Describe the morphology of the erythrocytes.
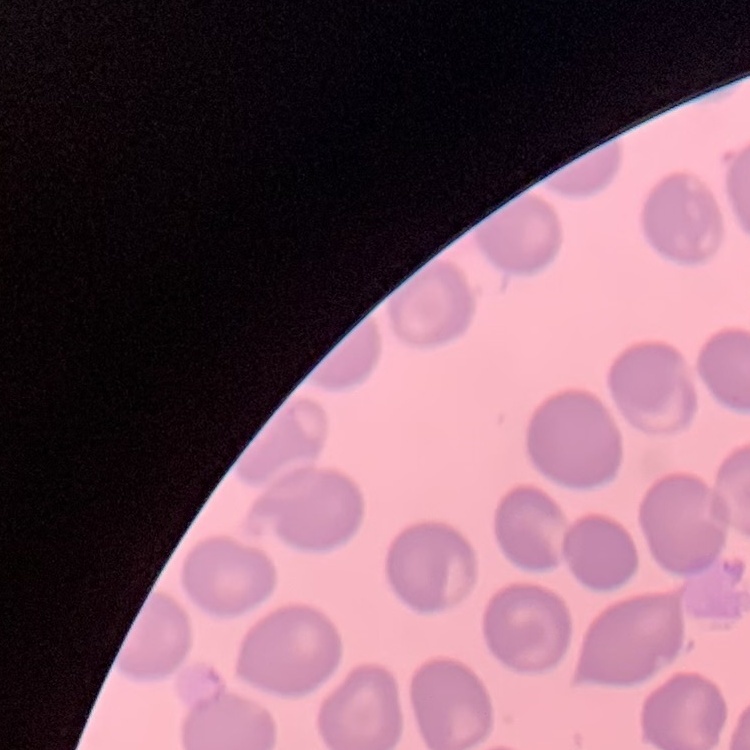

No rouleaux formation.

Thin peripheral smear. Field's or Giemsa stain. Square crop of a larger photomicrograph.